State which cell type is depicted.
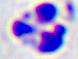
A leukocyte.

Photomicrograph. 400x magnification.